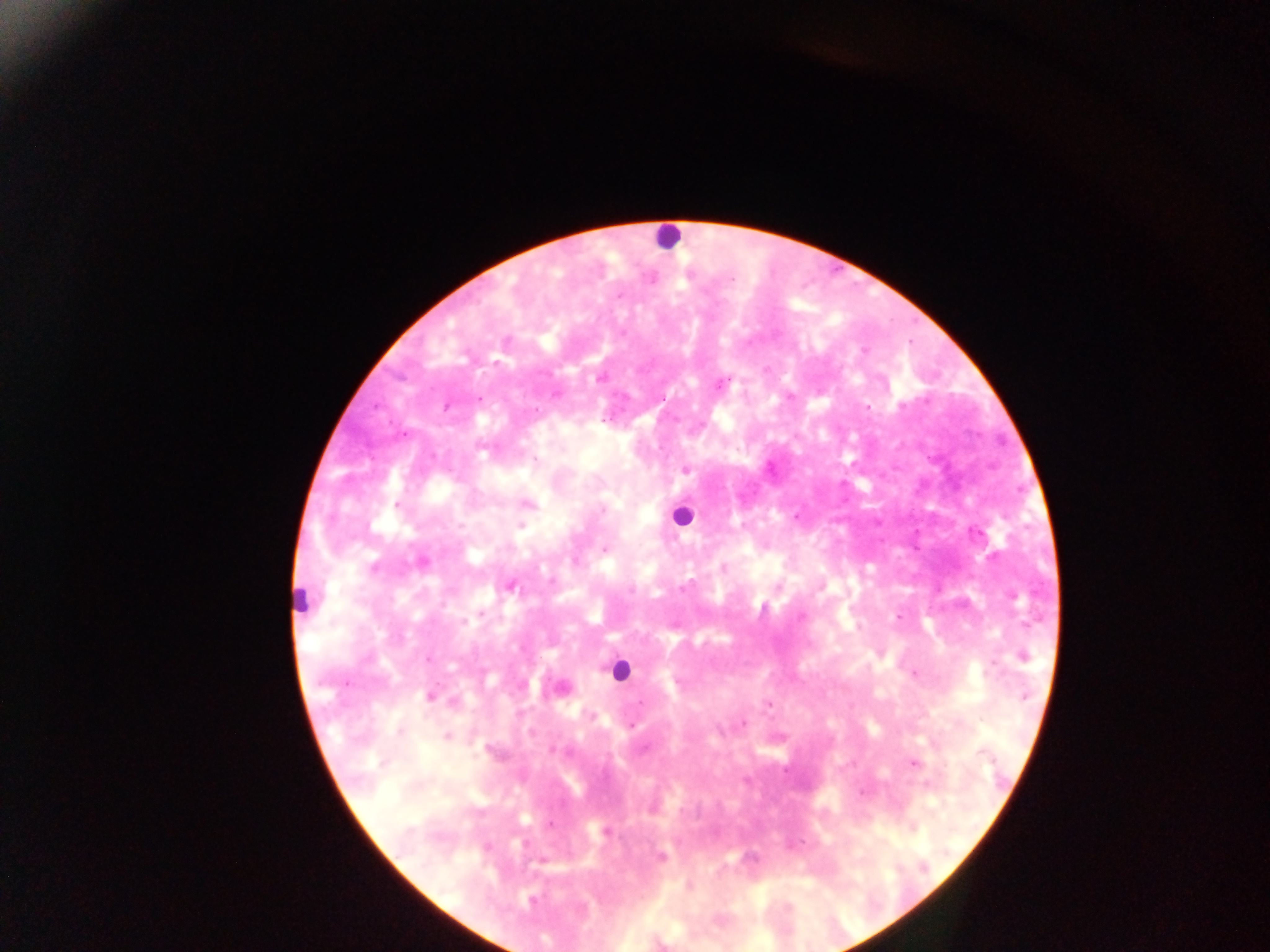

{
  "capture": "mobile-phone photograph through a microscope",
  "preparation": "thick blood smear",
  "field_of_view": "single",
  "leukocyte_locations": "approximate centers as [x, y] in pixels: [667, 236], [681, 516], [300, 599], [619, 671]",
  "country": "Ghana",
  "image_size": "1270×952 pixels",
  "malaria_parasite_locations": "approximate centers as [x, y] in pixels: [730, 278], [619, 295], [864, 351], [599, 379], [724, 382], [789, 397], [662, 398], [478, 399], [447, 406], [902, 406], [867, 407], [535, 459], [685, 470], [527, 504], [396, 505], [603, 510], [796, 517], [520, 525], [604, 549], [422, 562], [374, 567], [723, 568], [510, 587], [684, 587], [632, 591], [481, 613], [801, 616], [898, 617], [464, 621], [1022, 657], [429, 658], [914, 674], [430, 697], [639, 702], [767, 705], [744, 722], [631, 725], [400, 732], [447, 737], [982, 753], [913, 763], [861, 792], [550, 824], [605, 832], [662, 857], [532, 900]"
}